Locate platelets.
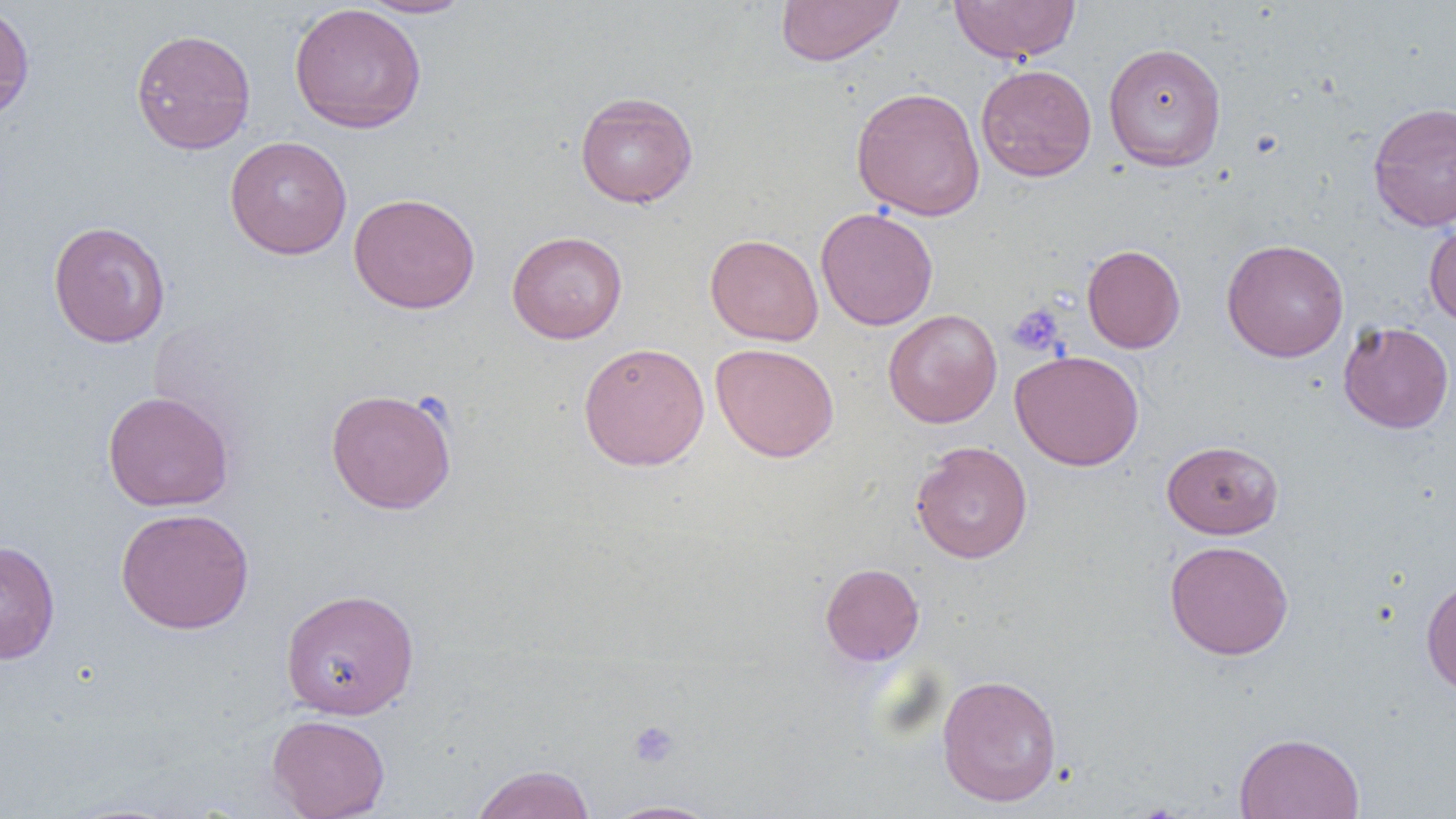
Approximate bounding boxes as (x1,y1)-(x2,y2) corner pairs in pixels.
Platelets: (1008,303)-(1066,356), (627,720)-(681,769).

slide-level diagnosis = no evidence of blood parasites
magnification = 1000x
modality = light microscopy
image size = 1456×819 pixels
uninfected red blood cell locations = approximate bounding boxes as (x1,y1)-(x2,y2) corner pairs in pixels: (355,0)-(476,19), (774,0)-(906,66), (949,0)-(1082,64), (0,3)-(35,123), (288,3)-(427,134), (130,28)-(257,154), (1103,42)-(1226,171), (975,63)-(1096,182), (850,86)-(986,221), (574,90)-(699,208), (1367,101)-(1456,232), (224,136)-(352,259), (348,193)-(480,314), (815,207)-(939,331), (1423,216)-(1456,328), (47,220)-(171,348), (506,231)-(628,343), (705,233)-(824,346), (1222,238)-(1349,362), (1082,244)-(1186,353), (883,309)-(1002,427), (1338,321)-(1454,434), (578,341)-(710,471), (710,342)-(839,463), (1010,349)-(1144,471), (325,387)-(457,514), (102,390)-(235,512), (1161,439)-(1284,539), (911,441)-(1033,563), (115,507)-(255,634), (0,540)-(60,665), (1164,540)-(1294,660), (820,563)-(924,666), (1421,575)-(1456,699), (280,588)-(420,719), (937,673)-(1062,807), (267,714)-(390,819), (1234,731)-(1365,819), (469,764)-(596,819), (602,800)-(721,819)
field of view = single
preparation = thin blood smear